Point out malaria parasites and leukocytes.
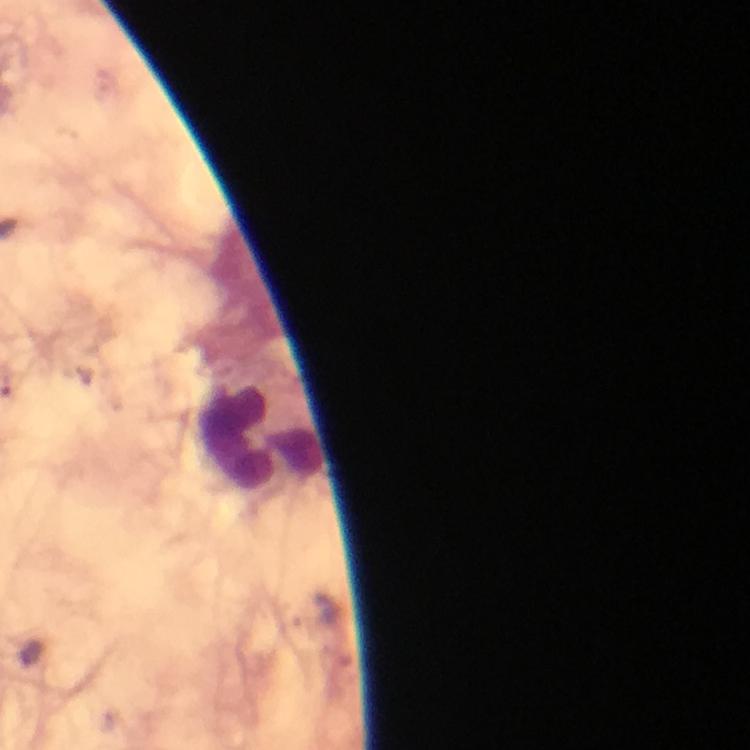
No malaria parasites seen.
Approximate object centers, in pixels from the top-left corner.
Leukocytes: (x=259, y=437).

Giemsa-stained preparation. From a diagnostic examination for malaria. Thick blood film. Image is 750×750 pixels. A crop from one field of view. Photographed through the microscope with a smartphone camera. Immersion oil applied. At 100x magnification.